Locate and identify every blood parasite.
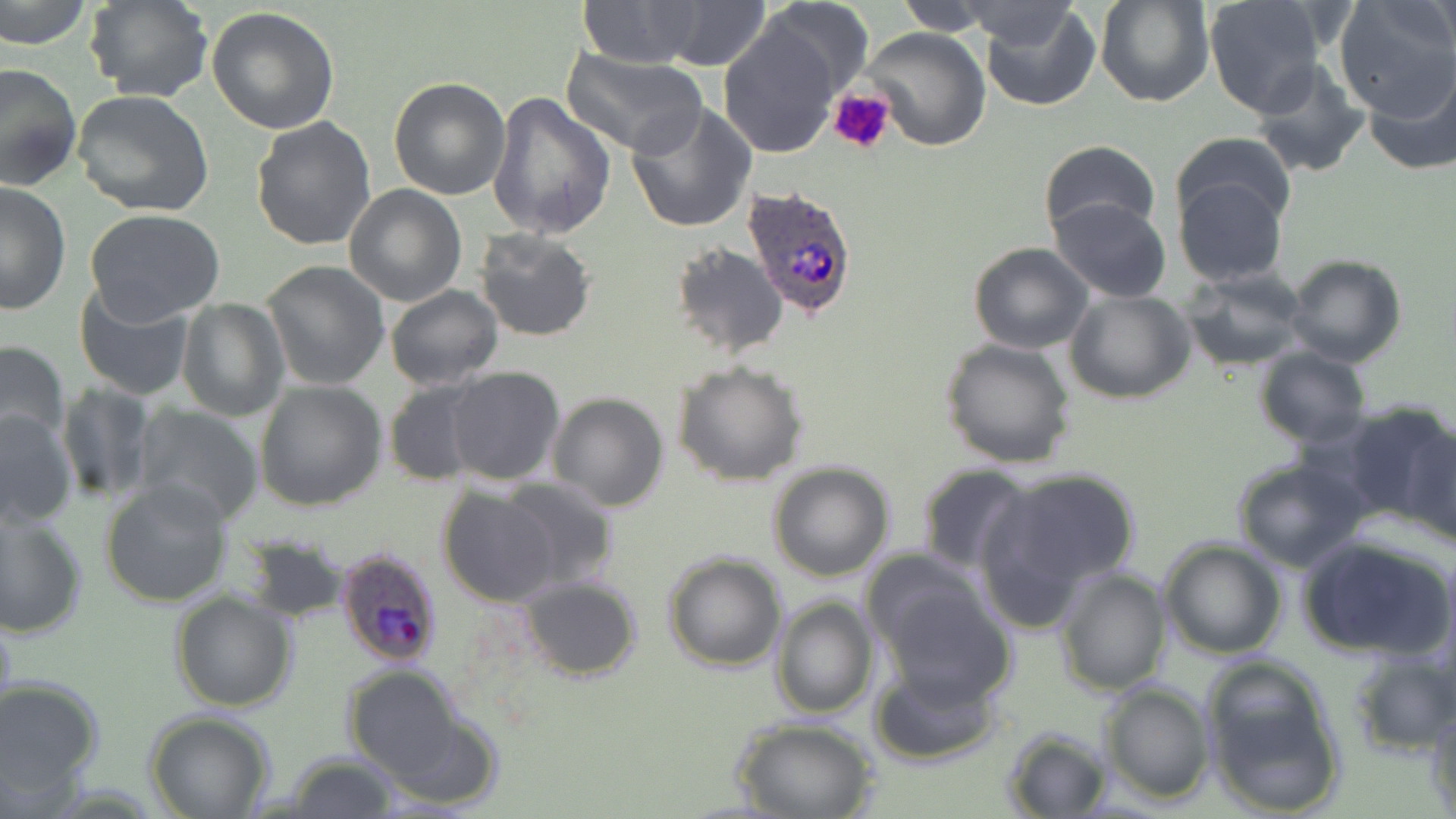
Approximate bounding boxes as [x1, y1, x2, y2] in pixels.
Plasmodium ovale-infected red blood cells: [745, 186, 860, 322], [334, 548, 443, 669].
No Plasmodium falciparum, Plasmodium malariae, Plasmodium vivax, Babesia divergens, or Trypanosoma brucei observed.

slide-level diagnosis = Plasmodium ovale
preparation = thin blood smear
stain = May-Grünwald-Giemsa
uninfected red blood cell locations = approximate bounding boxes as [x1, y1, x2, y2] in pixels: [0, 0, 93, 51], [85, 0, 215, 105], [575, 0, 707, 68], [757, 0, 875, 105], [891, 0, 1004, 35], [1095, 0, 1213, 106], [1204, 0, 1327, 117], [959, 1, 1085, 51], [978, 1, 1100, 112], [1331, 1, 1456, 119], [656, 2, 771, 70], [207, 6, 340, 134], [716, 16, 845, 159], [863, 27, 992, 150], [560, 48, 706, 158], [1249, 61, 1372, 179], [1363, 61, 1456, 176], [0, 62, 81, 192], [388, 77, 511, 200], [72, 91, 214, 217], [487, 92, 616, 240], [624, 101, 756, 232], [251, 115, 378, 251], [1170, 131, 1298, 238], [1038, 140, 1160, 242], [1173, 173, 1290, 288], [0, 181, 71, 314], [344, 185, 468, 306], [1050, 196, 1171, 303], [82, 210, 227, 323], [473, 227, 599, 343], [967, 241, 1093, 354], [669, 242, 787, 358], [1284, 254, 1407, 370], [259, 260, 390, 391], [1180, 268, 1310, 370], [73, 282, 197, 401], [384, 285, 504, 390], [1066, 290, 1195, 404], [177, 298, 287, 422], [941, 337, 1077, 469], [0, 339, 70, 450], [1254, 347, 1370, 447], [672, 359, 809, 486], [444, 366, 565, 486], [383, 379, 489, 486], [56, 380, 155, 504], [254, 381, 387, 512], [548, 392, 670, 512], [1345, 403, 1454, 532], [132, 405, 264, 526], [0, 408, 78, 528], [1403, 427, 1456, 550], [1229, 456, 1372, 572], [768, 462, 894, 582], [915, 462, 1036, 574], [988, 467, 1141, 601], [494, 476, 621, 594], [102, 477, 234, 607], [437, 488, 561, 607], [0, 506, 88, 641], [1296, 532, 1454, 663], [245, 534, 351, 624], [1158, 538, 1286, 659], [661, 552, 787, 673], [864, 554, 1004, 691], [1053, 566, 1173, 697], [515, 577, 642, 680], [170, 589, 296, 713], [770, 595, 878, 718], [0, 604, 19, 740], [1344, 649, 1456, 756], [1200, 657, 1346, 816], [343, 664, 468, 785], [868, 664, 1004, 767], [0, 678, 103, 803], [1098, 681, 1214, 803], [1426, 705, 1456, 818], [145, 712, 274, 819], [733, 717, 880, 819], [1001, 727, 1111, 816], [283, 753, 402, 819]
modality = light microscopy
magnification = 1000x
field of view = one of a larger specimen
platelet locations = approximate bounding boxes as [x1, y1, x2, y2] in pixels: [829, 88, 895, 155]
image size = 1456×819 pixels